Give a bounding box for every leukocyte visible.
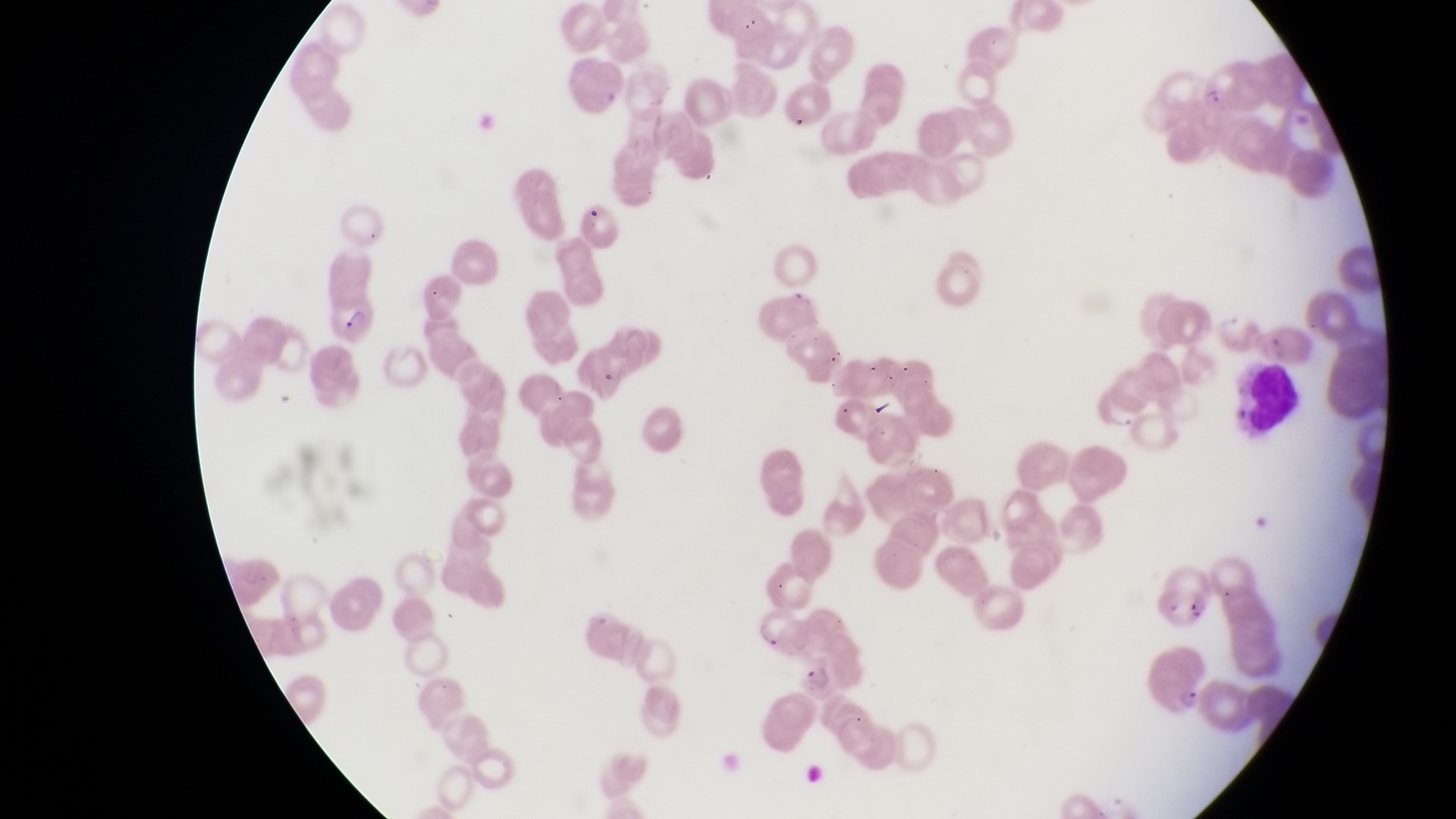
Approximate bounding boxes as [left, top, right, bottom] in pixels.
Leukocytes: [1242, 359, 1313, 442].

Parasitised red blood cell locations: [320, 291, 383, 344], [752, 612, 800, 649], [1139, 645, 1215, 717], [793, 651, 853, 704]. Artifact (platelet-like body, stain precipitate, or debris) locations: [1146, 584, 1210, 627]. Photographed through the eyepiece of an Olympus CX-23 microscope with a smartphone camera. One field of view. Image is 1456×819 pixels. Sample from Uganda. Thin blood film. Magnification of 1000x.